Locate every uninfected red blood cell.
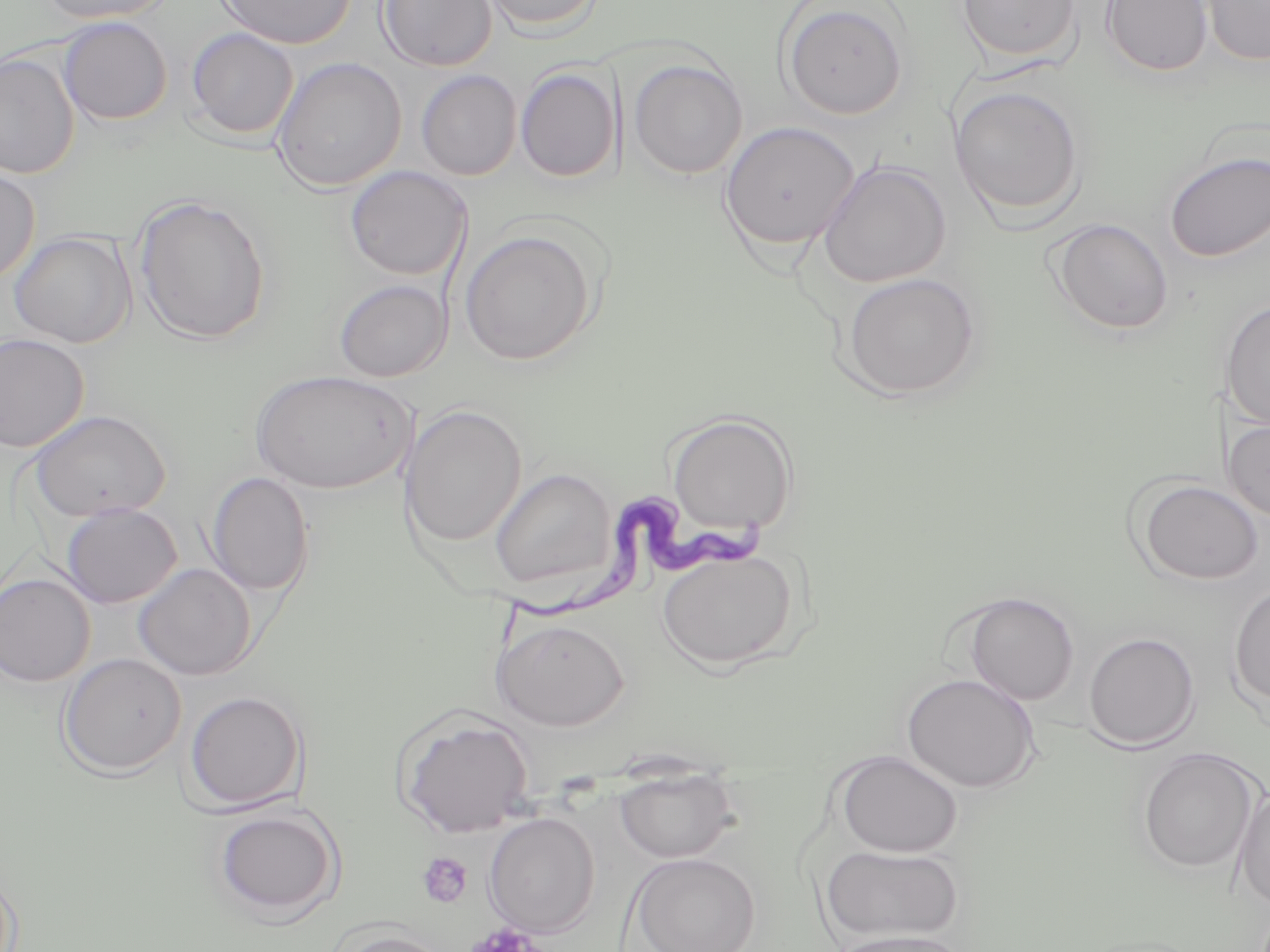
Approximate bounding boxes as named x1/y1/x2/y2 corners in pixels.
Uninfected red blood cells: (x1=34, y1=0, x2=175, y2=24), (x1=215, y1=0, x2=357, y2=50), (x1=376, y1=0, x2=497, y2=72), (x1=480, y1=0, x2=604, y2=35), (x1=955, y1=0, x2=1083, y2=65), (x1=1100, y1=0, x2=1213, y2=77), (x1=1200, y1=0, x2=1270, y2=67), (x1=779, y1=1, x2=910, y2=120), (x1=57, y1=16, x2=173, y2=126), (x1=186, y1=27, x2=299, y2=140), (x1=0, y1=52, x2=80, y2=179), (x1=271, y1=56, x2=406, y2=193), (x1=628, y1=58, x2=748, y2=179), (x1=515, y1=67, x2=620, y2=183), (x1=416, y1=69, x2=522, y2=180), (x1=949, y1=84, x2=1086, y2=222), (x1=719, y1=121, x2=861, y2=251), (x1=1163, y1=151, x2=1270, y2=262), (x1=818, y1=160, x2=952, y2=288), (x1=0, y1=165, x2=40, y2=285), (x1=345, y1=165, x2=472, y2=280), (x1=133, y1=194, x2=271, y2=345), (x1=1049, y1=218, x2=1174, y2=335), (x1=459, y1=229, x2=596, y2=366), (x1=8, y1=231, x2=136, y2=348), (x1=840, y1=272, x2=983, y2=401), (x1=333, y1=279, x2=451, y2=382), (x1=1221, y1=299, x2=1270, y2=430), (x1=0, y1=333, x2=90, y2=452), (x1=250, y1=369, x2=414, y2=494), (x1=400, y1=404, x2=527, y2=549), (x1=30, y1=409, x2=171, y2=522), (x1=667, y1=412, x2=798, y2=536), (x1=1223, y1=418, x2=1270, y2=522), (x1=489, y1=466, x2=617, y2=594), (x1=205, y1=472, x2=314, y2=597), (x1=1134, y1=478, x2=1265, y2=585), (x1=60, y1=503, x2=182, y2=608), (x1=655, y1=546, x2=799, y2=670), (x1=133, y1=563, x2=257, y2=680), (x1=0, y1=573, x2=95, y2=687), (x1=1228, y1=581, x2=1270, y2=710), (x1=959, y1=592, x2=1080, y2=706), (x1=491, y1=617, x2=630, y2=730), (x1=1082, y1=631, x2=1200, y2=750), (x1=58, y1=652, x2=186, y2=777), (x1=901, y1=672, x2=1041, y2=793), (x1=183, y1=689, x2=307, y2=813), (x1=393, y1=708, x2=535, y2=839), (x1=1136, y1=747, x2=1262, y2=875), (x1=834, y1=751, x2=963, y2=857), (x1=614, y1=771, x2=741, y2=863), (x1=1230, y1=786, x2=1270, y2=910), (x1=212, y1=806, x2=343, y2=922), (x1=483, y1=812, x2=600, y2=938), (x1=821, y1=844, x2=965, y2=945), (x1=628, y1=852, x2=760, y2=952), (x1=331, y1=929, x2=453, y2=951), (x1=826, y1=930, x2=974, y2=952).

{
  "slide_level_diagnosis": "Trypanosoma brucei",
  "modality": "light microscopy",
  "stain": "May-Grünwald-Giemsa",
  "field_of_view": "one of a larger specimen",
  "magnification": "1000x",
  "platelet_locations": "approximate bounding boxes as named x1/y1/x2/y2 corners in pixels: (x1=417, y1=852, x2=474, y2=909), (x1=466, y1=923, x2=544, y2=952)",
  "image_size": "1270×952 pixels",
  "trypanosoma_brucei_locations": "approximate bounding boxes as named x1/y1/x2/y2 corners in pixels: (x1=498, y1=493, x2=779, y2=651)",
  "preparation": "thin blood smear"
}